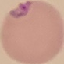
Summary:
  - Malaria status: parasitized
  - Image type: cell patch, automatically extracted from a larger field of view and resized to 64 × 64 pixels
  - Stain: Giemsa
  - Capture: smartphone through the microscope eyepiece
  - Preparation: thin smear